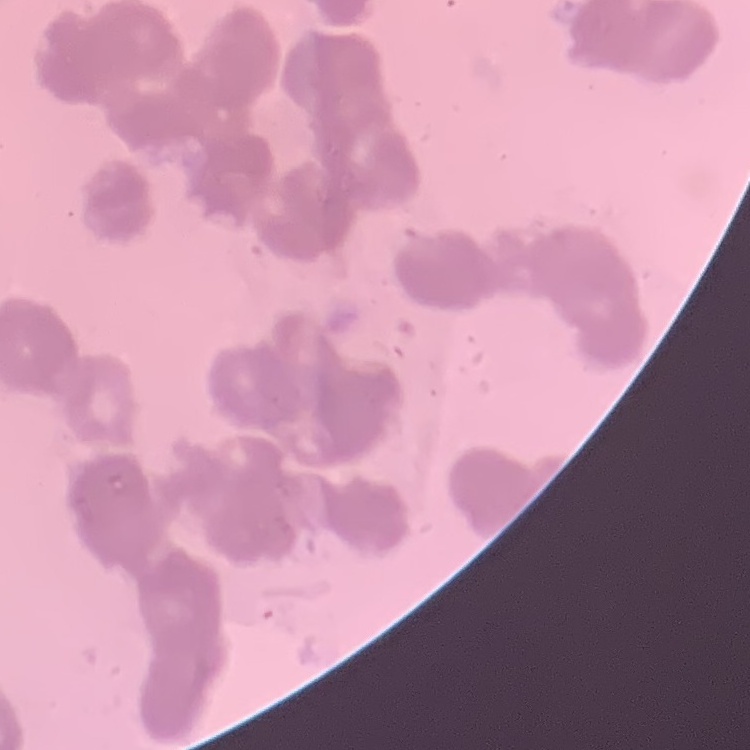
Summary:
  - Red blood cell morphology: rouleaux formation
  - Preparation: thin blood film
  - Stain: Field's or Giemsa
  - Image type: one tile cut from a larger photomicrograph